Name the cell type shown.
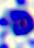

This is a leukocyte.

{
  "modality": "micrograph",
  "magnification": "400x"
}